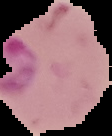
preparation = thin blood film
image size = 112×136 pixels
malaria status = parasitized
image type = segmented cell region on a black background